Describe the morphology of the erythrocytes.
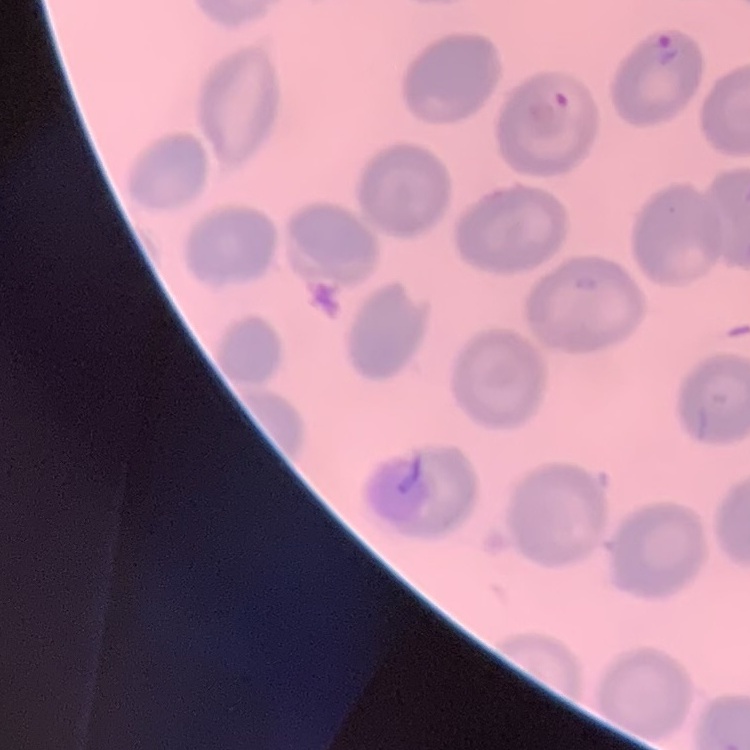

No rouleaux formation.

Summary:
  - Image type: one tile cut from a larger photomicrograph
  - Stain: Field's or Giemsa
  - Preparation: thin blood film